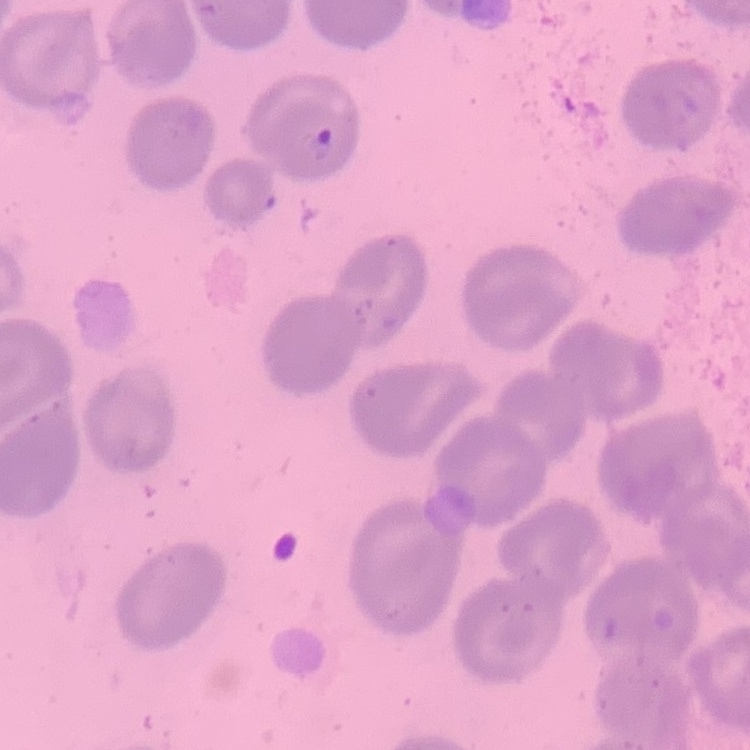
red blood cell morphology = no rouleaux formation
stain = Field's or Giemsa
image type = one tile cut from a larger photomicrograph
preparation = thin peripheral smear